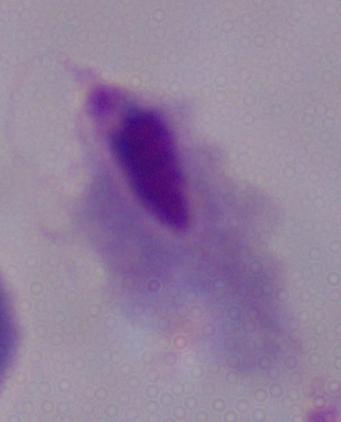

modality = photomicrograph
identification = trichomonad
magnification = 1000x